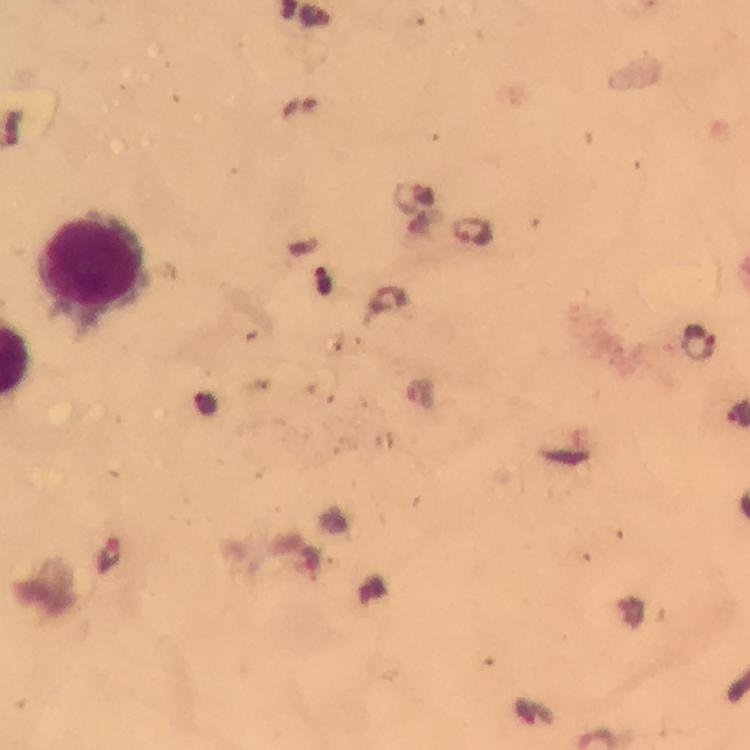
Approximate centers as (x, y) in pixels. Leukocyte locations: (89, 264). Plasmodium parasite locations: (471, 230), (697, 340), (421, 394), (109, 555). Thick blood film. Giemsa-stained preparation. Immersion oil was used. Photographed with a smartphone mounted on the microscope. A crop from one field of view. From a malaria diagnostic workup. Image is 750×750 pixels. At 100x magnification.